Report the malaria status of this cell.
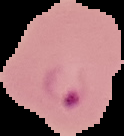
Parasitized.

Summary:
  - Image type: cell region segmented out of the field of view; surrounding area masked to black
  - Preparation: thin blood film
  - Image size: 124×136 pixels